Classify this cell by malaria status.
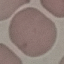
Uninfected.

Summary:
  - Image type: automatically extracted cell patch, resized to 64 × 64 pixels
  - Preparation: thin smear
  - Stain: Giemsa
  - Capture: smartphone through the microscope eyepiece